Assess this cell for malaria.
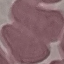
It is uninfected.

Summary:
  - Capture: smartphone camera at the microscope eyepiece
  - Image type: automatically extracted cell patch, resized to 64 × 64 pixels
  - Preparation: thin smear
  - Stain: Giemsa